State which parasite is depicted.
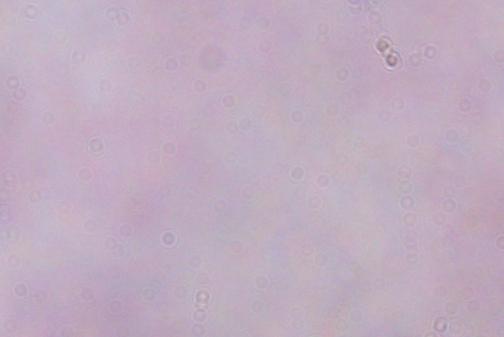
A trypanosome.

{
  "modality": "micrograph",
  "magnification": "1000x"
}